Identify the parasite.
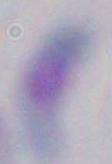
This is Toxoplasma gondii.

Captured at 1000x magnification. Photomicrograph.